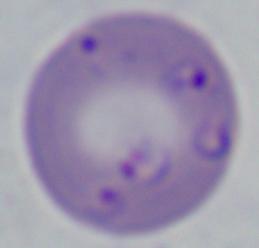

A Babesia parasite is seen. 1000x magnification. Photomicrograph.